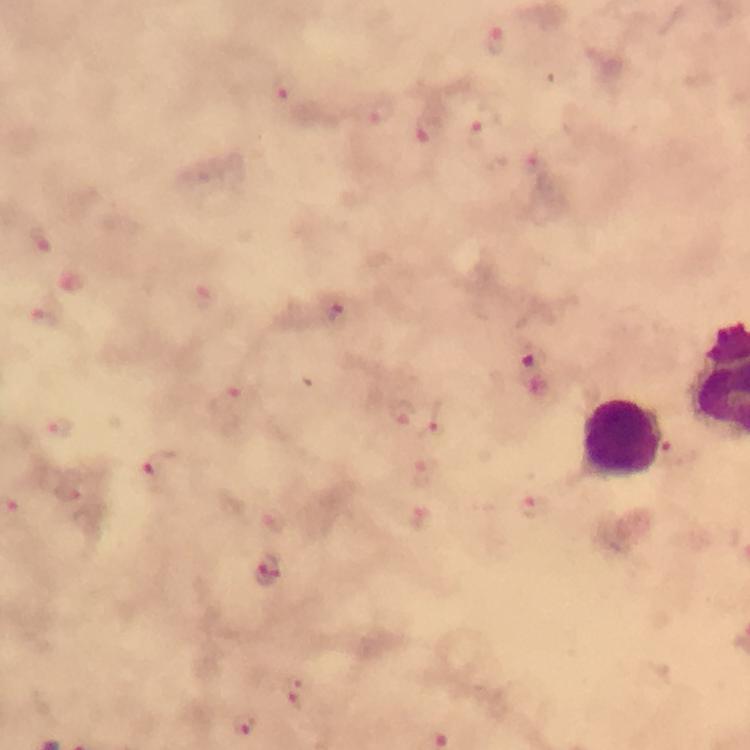
Approximate object centers, in pixels from the top-left corner.
Summary:
  - Malaria parasite locations: (x=497, y=40), (x=284, y=87), (x=382, y=110), (x=429, y=135), (x=477, y=138), (x=531, y=161), (x=43, y=237), (x=207, y=296), (x=335, y=310), (x=46, y=315), (x=530, y=355), (x=231, y=399), (x=403, y=412), (x=434, y=424), (x=59, y=429), (x=676, y=453), (x=158, y=467), (x=425, y=472), (x=532, y=508), (x=422, y=522), (x=266, y=572), (x=297, y=696), (x=248, y=724)
  - Leukocyte locations: (x=619, y=441)
  - Cropped from: one field of view
  - Stain: Giemsa
  - Magnification: 100x
  - Capture: smartphone photograph through a microscope
  - Immersion oil: applied
  - Image size: 750×750 pixels
  - Preparation: thick blood smear
  - Context: from a diagnostic examination for malaria